Assess this cell for malaria.
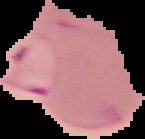
It is parasitized.

{
  "preparation": "thin blood film",
  "image_size": "145×139 pixels",
  "image_type": "cell region segmented out of the field of view; surrounding area masked to black"
}